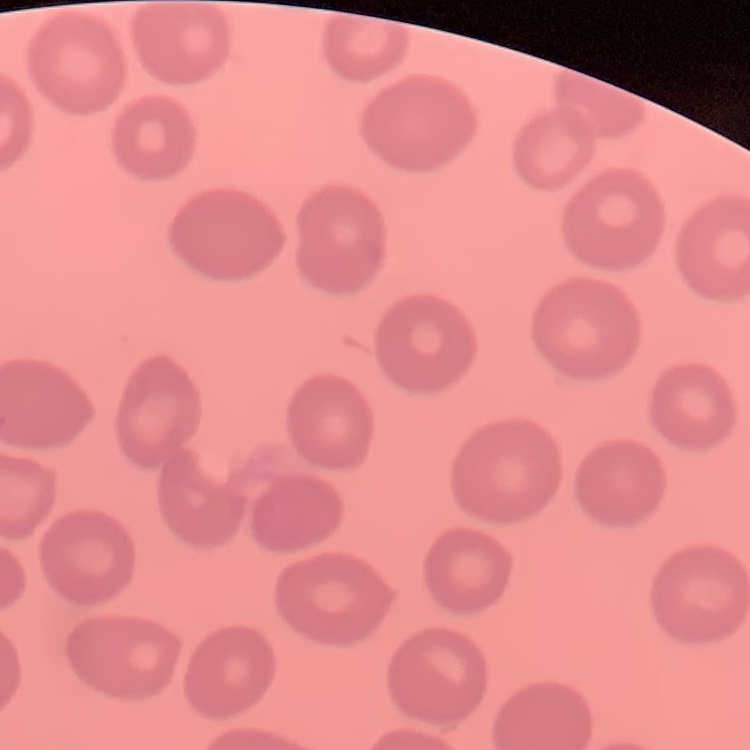

Summary:
  - Erythrocyte morphology: no rouleaux formation
  - Image type: square crop of a larger photomicrograph
  - Stain: Field's or Giemsa
  - Preparation: thin blood smear